Give the extent of all Plasmodium falciparum-infected red blood cells.
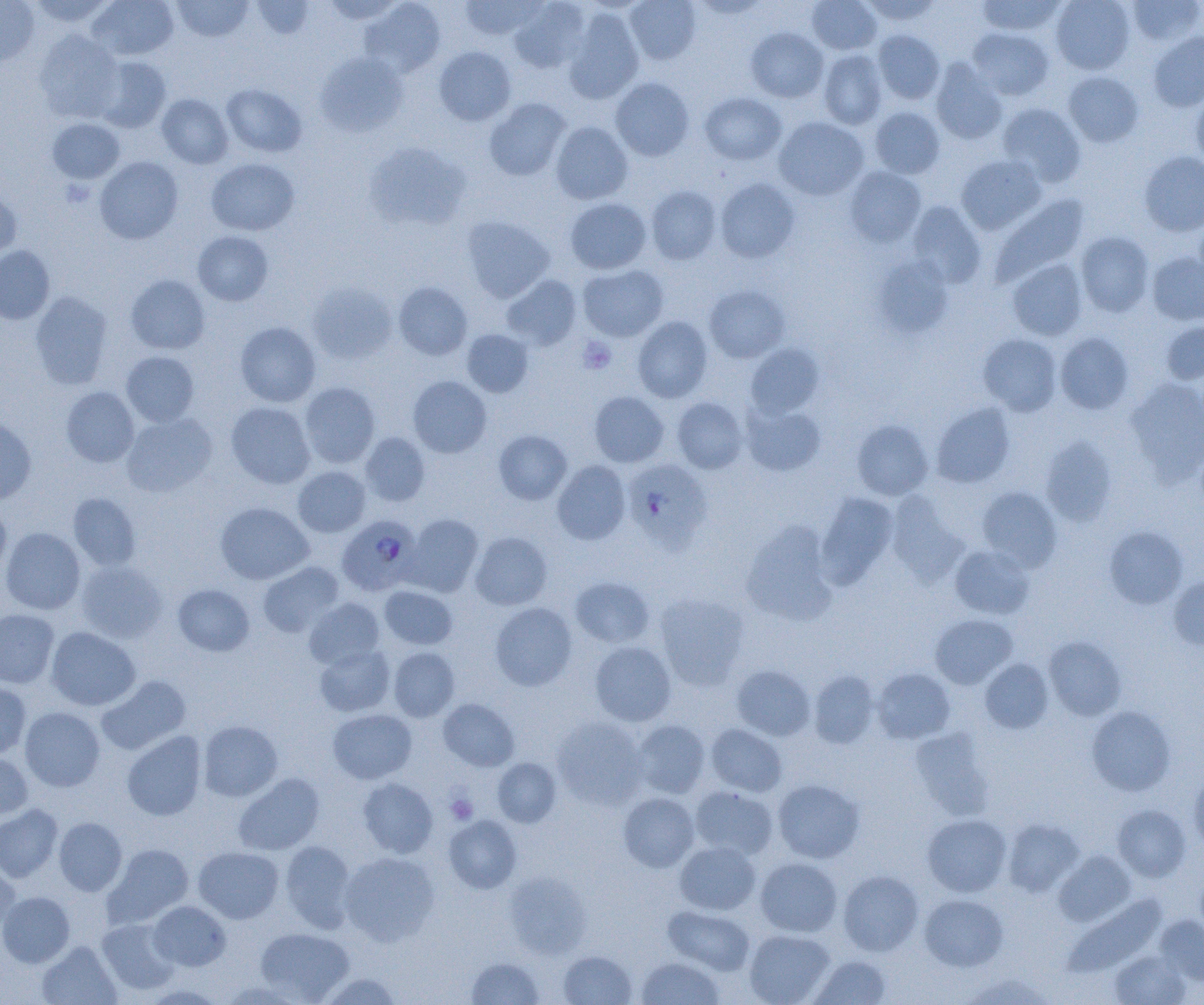
Approximate bounding boxes as [x1, y1, x2, y2] in pixels.
Plasmodium falciparum-infected red blood cells: [623, 459, 712, 553], [337, 515, 423, 596].

Summary:
  - Platelet locations: [578, 337, 616, 373], [445, 792, 479, 825]
  - Uninfected red blood cell locations: [26, 0, 117, 28], [87, 0, 179, 60], [172, 0, 253, 42], [251, 0, 314, 39], [321, 0, 406, 23], [460, 0, 545, 41], [509, 0, 591, 73], [624, 0, 701, 65], [690, 0, 771, 19], [807, 0, 881, 54], [860, 0, 942, 26], [977, 0, 1066, 36], [1051, 0, 1135, 74], [1126, 0, 1204, 47], [0, 1, 39, 68], [360, 1, 447, 78], [563, 9, 644, 104], [746, 27, 829, 102], [967, 27, 1053, 100], [34, 30, 123, 122], [872, 30, 945, 103], [1148, 31, 1204, 112], [433, 46, 516, 126], [819, 50, 888, 129], [315, 52, 409, 136], [93, 56, 171, 132], [931, 58, 1008, 145], [1063, 72, 1144, 147], [610, 77, 694, 161], [221, 83, 307, 157], [700, 92, 787, 165], [1191, 92, 1204, 169], [157, 94, 233, 169], [484, 98, 571, 181], [996, 103, 1086, 187], [869, 107, 944, 179], [774, 117, 868, 200], [47, 118, 124, 183], [550, 121, 633, 204], [364, 141, 471, 230], [1138, 150, 1204, 237], [956, 155, 1047, 234], [94, 156, 183, 244], [206, 158, 300, 235], [844, 166, 926, 247], [715, 178, 800, 263], [646, 185, 722, 265], [0, 187, 22, 261], [990, 194, 1090, 287], [565, 197, 652, 274], [906, 201, 986, 288], [1194, 215, 1204, 288], [461, 216, 554, 302], [192, 231, 274, 306], [1076, 231, 1154, 317], [0, 245, 55, 324], [1147, 252, 1204, 325], [873, 255, 955, 338], [1007, 258, 1087, 341], [577, 264, 669, 341], [125, 274, 210, 355], [501, 274, 581, 350], [307, 281, 397, 364], [393, 282, 472, 360], [705, 285, 789, 363], [30, 291, 113, 389], [633, 316, 712, 402], [235, 321, 320, 407], [1160, 321, 1204, 385], [461, 329, 533, 397], [1055, 332, 1134, 414], [978, 333, 1062, 416], [745, 343, 824, 418], [121, 351, 200, 426], [408, 376, 491, 458], [1125, 377, 1204, 484], [299, 382, 380, 468], [60, 386, 139, 467], [589, 391, 669, 467], [672, 397, 748, 474], [226, 402, 315, 488], [741, 403, 826, 476], [931, 403, 1015, 488], [121, 412, 218, 497], [0, 418, 37, 504], [851, 419, 933, 500], [493, 430, 572, 504], [360, 432, 430, 506], [1040, 436, 1117, 526], [552, 460, 631, 544], [293, 466, 371, 537], [977, 486, 1062, 571], [816, 492, 898, 588], [886, 492, 968, 586], [68, 493, 141, 570], [216, 502, 314, 584], [0, 503, 11, 578], [404, 514, 484, 596], [740, 521, 838, 626], [1105, 526, 1187, 609], [1, 527, 85, 614], [470, 532, 552, 610], [950, 544, 1035, 619], [76, 560, 168, 643], [258, 561, 344, 637], [1168, 575, 1204, 650], [570, 576, 655, 648], [173, 584, 254, 656], [379, 585, 457, 650], [654, 592, 750, 689], [304, 598, 385, 670], [490, 602, 577, 691], [0, 608, 59, 688], [930, 614, 1018, 689], [46, 626, 141, 710], [1043, 636, 1126, 720], [590, 641, 677, 726], [314, 644, 395, 717], [388, 647, 459, 721], [980, 659, 1053, 733], [731, 664, 815, 740], [872, 668, 955, 744], [808, 669, 880, 749], [97, 675, 191, 755], [0, 680, 32, 759], [438, 698, 520, 771], [1086, 706, 1176, 797], [20, 707, 105, 792], [327, 708, 417, 784], [551, 716, 648, 809], [631, 719, 710, 799], [198, 720, 283, 801], [706, 723, 787, 797], [910, 728, 994, 821], [122, 731, 207, 821], [0, 753, 34, 820], [492, 758, 561, 827], [1189, 769, 1204, 854], [233, 773, 324, 855], [358, 777, 439, 858], [772, 779, 865, 863], [689, 786, 779, 860], [618, 792, 700, 872], [0, 804, 63, 882], [1112, 804, 1191, 881], [922, 814, 1012, 897], [443, 815, 522, 893], [54, 817, 127, 896], [1002, 818, 1085, 896], [279, 840, 356, 932], [674, 840, 761, 915], [102, 843, 194, 928], [193, 846, 283, 924], [1054, 850, 1136, 926], [339, 851, 439, 945], [755, 857, 843, 937], [0, 861, 20, 933], [838, 870, 923, 956], [504, 871, 592, 958], [0, 891, 74, 967], [919, 894, 1008, 971], [1063, 894, 1166, 977], [148, 901, 231, 971], [663, 905, 756, 975], [1155, 915, 1204, 989], [97, 918, 180, 995], [255, 926, 354, 1003], [744, 929, 835, 1005], [37, 940, 121, 1005], [559, 950, 636, 1004], [1110, 950, 1189, 1005], [808, 955, 892, 1004], [466, 956, 545, 1004], [635, 956, 725, 1004], [317, 972, 404, 1004], [960, 973, 1053, 1004], [219, 980, 307, 1004], [142, 984, 227, 1004]
  - Slide-level diagnosis: Plasmodium falciparum
  - Preparation: thin blood smear
  - Image size: 1204×1005 pixels
  - Modality: optical microscopy
  - Field of view: one of a larger specimen
  - Magnification: 1000x